Locate every leukocyte (white blood cell).
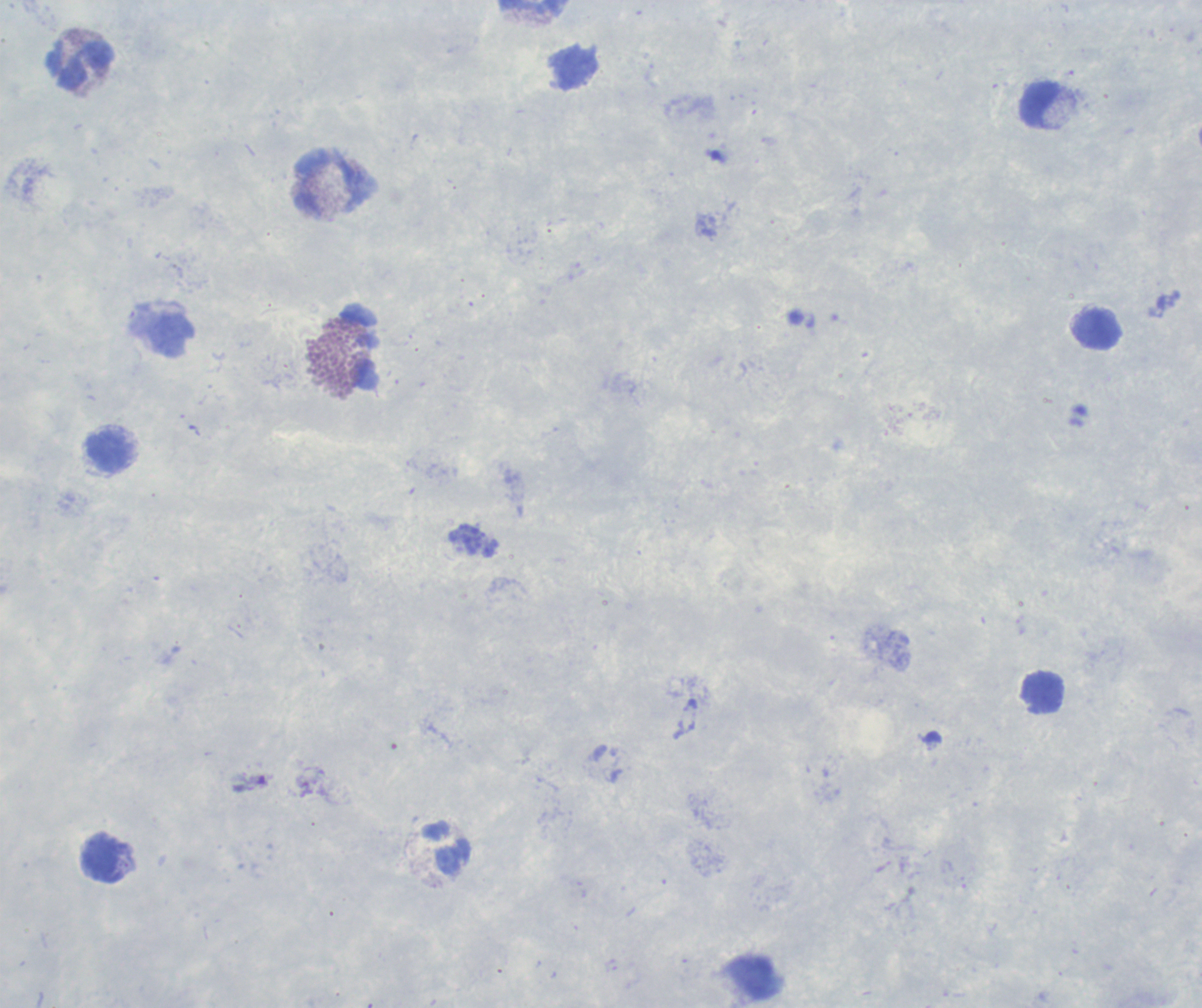
Approximate centers as [x, y] in pixels.
Leukocytes: [531, 7], [81, 65], [1041, 105], [333, 184], [1097, 330], [171, 335], [360, 348], [108, 454], [1043, 693], [447, 848], [105, 859].

magnification: 100x
field_of_view: one from this slide
preparation: thick smear of blood
background_quality: poor
coloration_quality: good
result: negative for Plasmodium parasites
context: previously used in an actual diagnosis
image_size: 1202×1008 pixels
stain: Romanowsky